State which parasite is depicted.
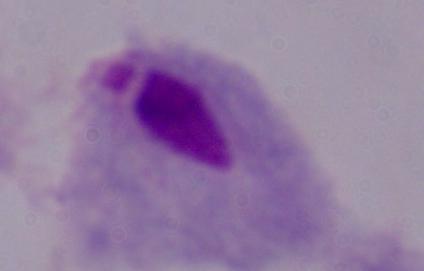
This is a trichomonad.

magnification = 1000x
modality = micrograph